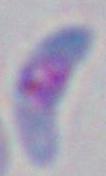

Micrograph. 1000x magnification. Toxoplasma gondii is seen.